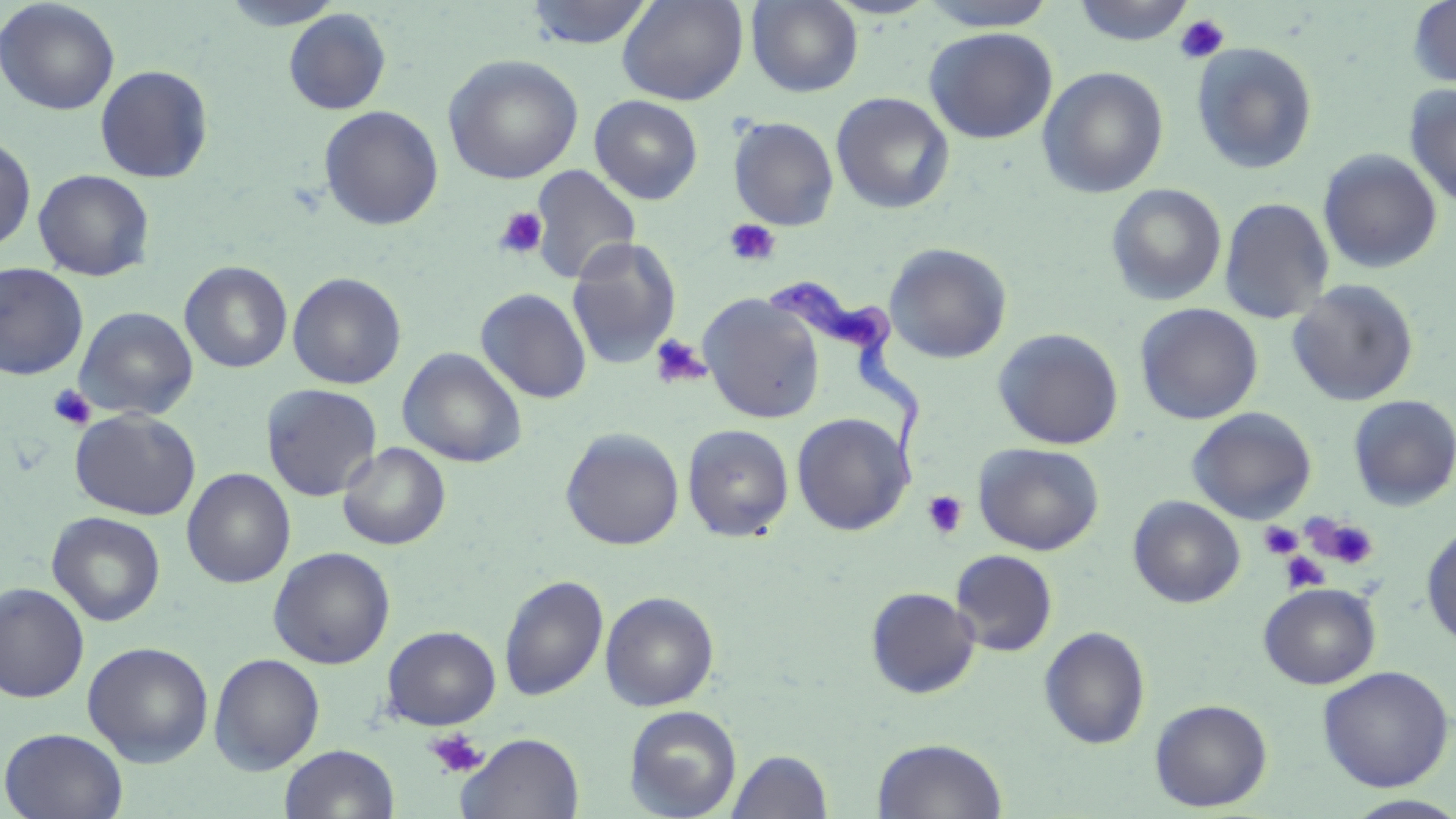

Approximate bounding boxes as (x1, y1, x2, y2) in pixels. Platelet locations: (1174, 14, 1230, 64), (494, 206, 548, 260), (724, 219, 781, 267), (649, 334, 711, 389), (48, 385, 97, 430), (922, 491, 968, 538), (1309, 515, 1380, 570), (1259, 521, 1303, 559), (1279, 551, 1329, 594), (425, 729, 489, 778). Trypanosoma brucei locations: (765, 276, 927, 489). Uninfected red blood cell locations: (220, 0, 345, 30), (617, 0, 748, 106), (916, 0, 1060, 31), (1071, 0, 1196, 46), (1408, 0, 1456, 89), (0, 1, 120, 115), (524, 1, 655, 49), (746, 1, 863, 97), (283, 8, 391, 114), (924, 27, 1058, 144), (1191, 42, 1318, 174), (443, 54, 583, 184), (95, 64, 213, 183), (1037, 66, 1169, 198), (1404, 83, 1456, 208), (831, 92, 955, 214), (589, 95, 703, 204), (318, 105, 443, 231), (729, 116, 840, 231), (0, 135, 36, 251), (1318, 149, 1442, 274), (529, 165, 641, 285), (33, 169, 155, 281), (1106, 183, 1226, 306), (1220, 198, 1334, 324), (566, 237, 683, 370), (884, 242, 1012, 364), (179, 261, 292, 374), (0, 262, 88, 380), (287, 272, 407, 389), (1287, 279, 1420, 407), (475, 288, 592, 404), (698, 295, 825, 424), (1135, 303, 1263, 425), (74, 306, 198, 421), (992, 328, 1124, 450), (397, 348, 527, 467), (261, 383, 382, 502), (1348, 395, 1456, 511), (1187, 407, 1317, 525), (70, 408, 200, 520), (63, 411, 182, 627), (792, 413, 914, 535), (682, 424, 794, 542), (560, 428, 685, 550), (338, 442, 451, 550), (974, 442, 1104, 555), (182, 468, 296, 588), (1128, 496, 1245, 608), (47, 511, 165, 626), (1421, 523, 1456, 650), (268, 546, 395, 669), (950, 550, 1058, 657), (498, 574, 609, 702), (0, 582, 90, 703), (1258, 583, 1381, 689), (866, 587, 981, 698), (600, 591, 719, 711), (381, 625, 501, 730), (1039, 626, 1151, 750), (82, 641, 214, 767), (209, 652, 325, 774), (1317, 665, 1454, 792), (1150, 698, 1272, 811), (624, 704, 742, 818), (1, 727, 129, 819), (457, 732, 584, 819), (873, 738, 1007, 819), (279, 744, 400, 819), (727, 749, 834, 819), (1343, 795, 1456, 818). Slide-level diagnosis: Trypanosoma brucei. Thin blood film. One field of a larger specimen. Image is 1456×819 pixels. Light microscopy. May-Grünwald-Giemsa-stained preparation. 1000x magnification.